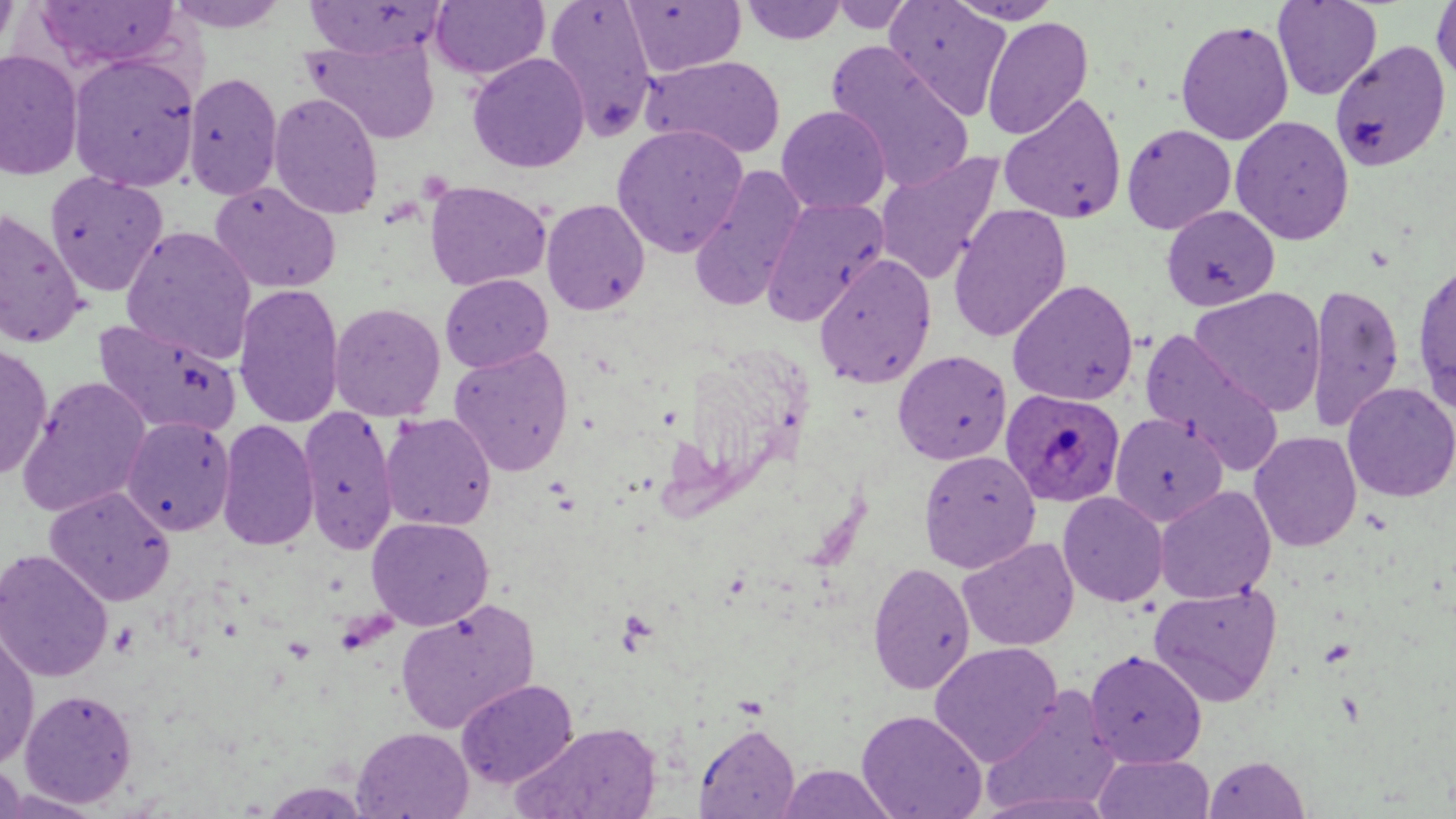
slide-level diagnosis = Plasmodium ovale
image size = 1456×819 pixels
preparation = thin blood film
field of view = one of a larger specimen
Plasmodium ovale-infected red blood cell locations = approximate bounding boxes as [x1, y1, x2, y2] in pixels: [1000, 388, 1126, 507]
uninfected red blood cell locations = approximate bounding boxes as [x1, y1, x2, y2] in pixels: [0, 0, 19, 59], [165, 0, 291, 33], [543, 0, 658, 142], [828, 0, 916, 33], [884, 0, 1011, 119], [945, 0, 1065, 26], [31, 1, 184, 73], [303, 1, 450, 60], [430, 1, 550, 81], [622, 1, 746, 77], [739, 1, 847, 45], [1272, 1, 1382, 100], [1431, 1, 1456, 88], [982, 17, 1094, 140], [1175, 19, 1294, 145], [302, 38, 440, 144], [1329, 39, 1452, 172], [826, 42, 976, 192], [0, 49, 84, 182], [467, 52, 589, 173], [67, 53, 200, 192], [641, 55, 787, 160], [183, 72, 283, 200], [268, 92, 384, 220], [998, 92, 1128, 224], [776, 105, 891, 214], [1230, 115, 1354, 245], [611, 124, 749, 257], [1121, 124, 1237, 234], [873, 151, 1004, 286], [689, 165, 808, 313], [44, 171, 168, 297], [209, 181, 341, 295], [424, 181, 551, 291], [760, 197, 889, 327], [540, 198, 650, 316], [948, 203, 1072, 343], [1161, 204, 1279, 311], [0, 207, 88, 350], [120, 226, 257, 364], [813, 253, 936, 388], [1412, 260, 1456, 414], [439, 273, 553, 374], [1007, 279, 1139, 406], [1306, 282, 1404, 432], [233, 283, 345, 429], [1189, 286, 1327, 416], [328, 302, 445, 421], [92, 317, 242, 439], [1139, 330, 1285, 475], [0, 341, 53, 480], [449, 345, 574, 477], [893, 350, 1012, 465], [17, 376, 151, 518], [1342, 382, 1456, 503], [298, 405, 398, 554], [379, 412, 497, 532], [1110, 412, 1228, 527], [121, 416, 235, 536], [216, 418, 319, 551], [1249, 431, 1362, 552], [918, 449, 1041, 573], [1154, 485, 1276, 604], [43, 486, 176, 607], [1058, 492, 1169, 607], [367, 517, 494, 631], [957, 537, 1079, 651], [0, 548, 114, 682], [867, 561, 976, 695], [1148, 583, 1283, 707], [394, 599, 540, 735], [0, 626, 39, 771], [929, 642, 1063, 767], [1084, 649, 1207, 768], [455, 678, 578, 788], [980, 686, 1123, 816], [20, 688, 138, 807], [856, 709, 988, 819], [510, 721, 663, 819], [695, 723, 800, 819], [351, 726, 474, 818], [1092, 753, 1215, 818], [1204, 755, 1310, 819], [0, 761, 26, 819], [777, 764, 898, 819]
magnification = 1000x
stain = May-Grünwald-Giemsa
modality = optical microscopy